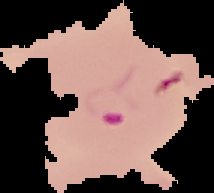
Image is 214×193 pixels. Malaria status: parasitized. From a thin blood smear. Segmented cell region on a black background.